Locate every blood parasite and identify its species.
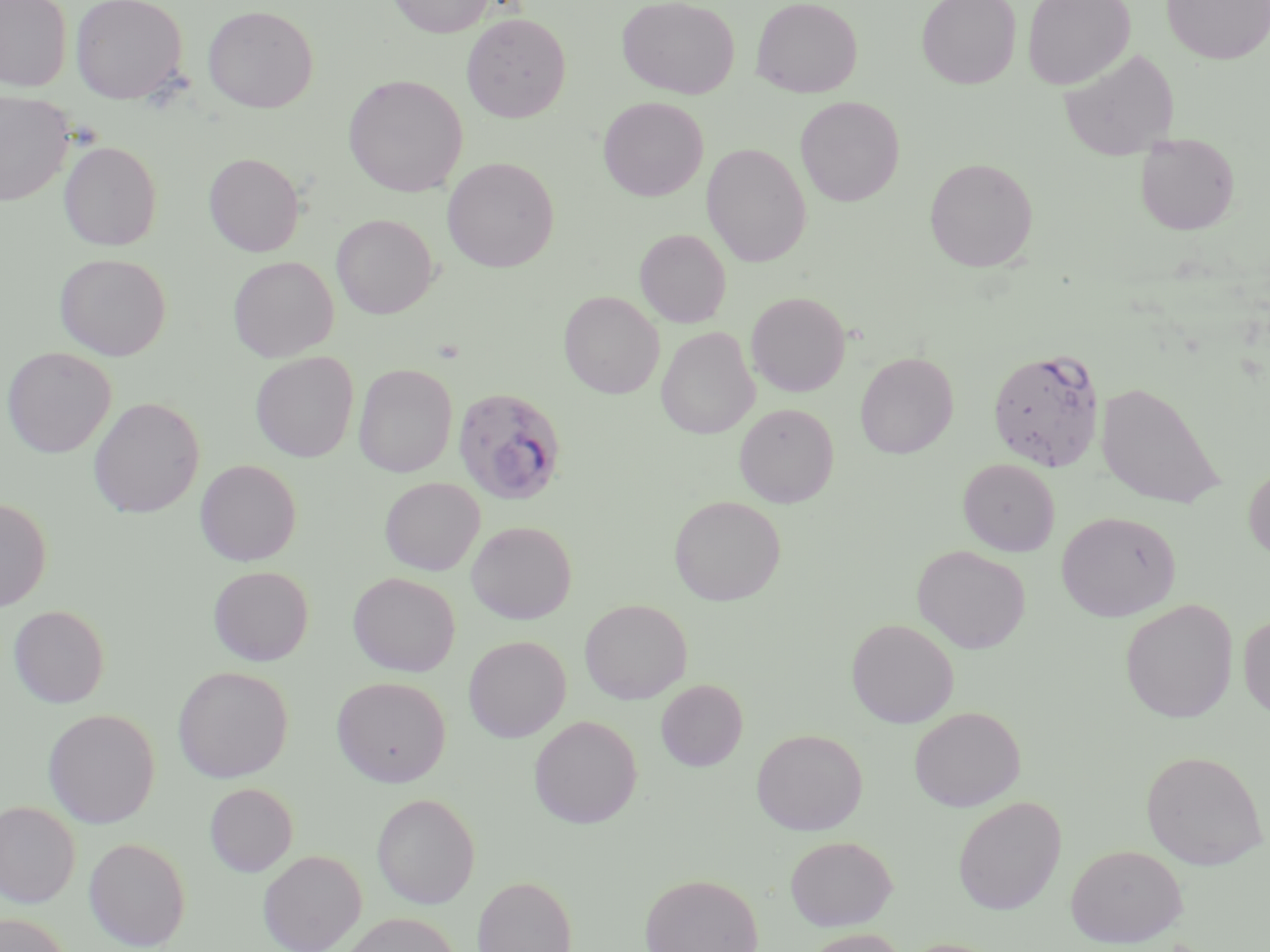

Approximate bounding boxes as [x1, y1, x2, y2] in pixels.
Plasmodium falciparum-infected red blood cells: [987, 347, 1105, 472], [453, 387, 568, 506].
No Plasmodium ovale, Plasmodium malariae, Plasmodium vivax, Babesia divergens, or Trypanosoma brucei observed.

slide_level_diagnosis: Plasmodium falciparum
modality: light microscopy
magnification: 1000x
preparation: thin blood smear
image_size: 1270×952 pixels
stain: May-Grünwald-Giemsa
uninfected_red_blood_cell_locations: 'approximate bounding boxes as [x1, y1, x2, y2] in pixels: [0, 0, 72, 91], [70, 0, 188, 104], [387, 0, 494, 37], [617, 0, 740, 99], [751, 0, 863, 98], [916, 0, 1021, 89], [1023, 0, 1135, 90], [1162, 0, 1270, 64], [203, 5, 319, 113], [461, 12, 571, 123], [1058, 48, 1179, 161], [344, 75, 467, 197], [0, 91, 74, 205], [795, 96, 905, 207], [599, 97, 708, 201], [1135, 133, 1239, 234], [59, 140, 162, 250], [702, 143, 811, 267], [205, 153, 304, 257], [442, 156, 559, 272], [924, 157, 1038, 272], [331, 214, 438, 318], [635, 228, 731, 327], [54, 253, 171, 360], [228, 256, 338, 361], [559, 291, 664, 399], [746, 291, 850, 396], [656, 326, 759, 439], [1, 346, 116, 457], [251, 351, 359, 462], [855, 351, 958, 458], [353, 363, 457, 478], [1095, 381, 1225, 510], [88, 396, 204, 518], [734, 403, 839, 507], [958, 458, 1060, 556], [196, 459, 302, 566], [1244, 463, 1270, 562], [380, 477, 485, 576], [669, 496, 785, 605], [0, 497, 52, 613], [1056, 510, 1180, 621], [466, 521, 576, 624], [912, 545, 1030, 653], [208, 565, 314, 666], [348, 572, 461, 676], [579, 599, 692, 704], [1119, 599, 1238, 723], [8, 605, 110, 708], [1238, 613, 1270, 721], [846, 618, 958, 728], [463, 635, 571, 742], [172, 666, 293, 783], [332, 676, 451, 787], [656, 679, 747, 771], [909, 706, 1025, 811], [42, 708, 160, 828], [529, 716, 642, 828], [751, 728, 868, 835], [1141, 750, 1268, 870], [204, 783, 298, 876], [371, 792, 480, 909], [953, 796, 1066, 915], [0, 800, 81, 907], [785, 835, 897, 930], [84, 837, 191, 950], [1065, 844, 1187, 947], [258, 849, 367, 952], [639, 873, 763, 952], [472, 875, 577, 952], [339, 912, 460, 952], [0, 913, 73, 952], [800, 928, 910, 952], [896, 938, 1006, 952]'
field_of_view: one of a larger specimen